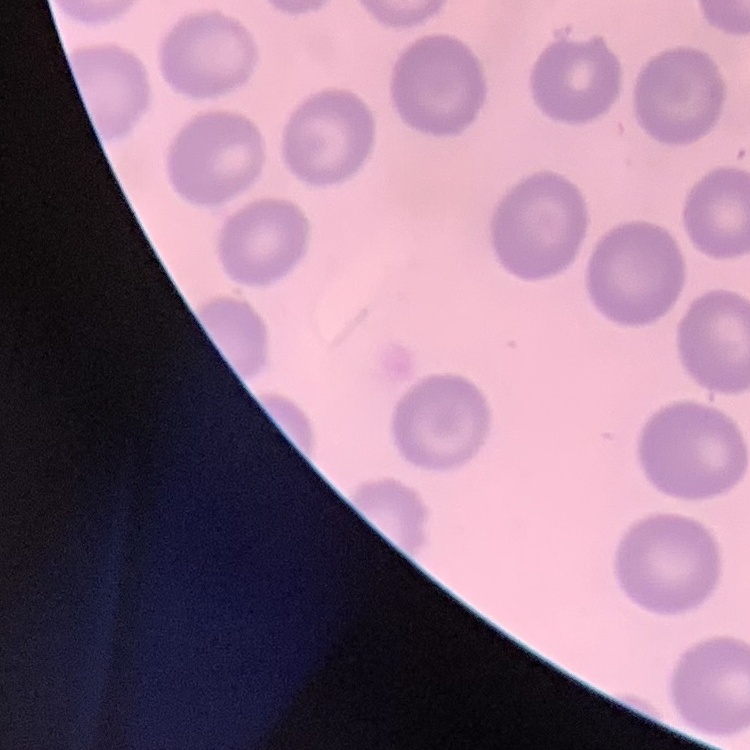
Summary:
  - Erythrocyte morphology: no rouleaux formation
  - Image type: square crop of a larger photomicrograph
  - Preparation: thin blood film
  - Stain: Field's or Giemsa